Assess this cell for malaria.
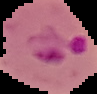
Parasitized.

preparation = thin blood film
image type = cell region segmented out of the field of view; surrounding area masked to black
image size = 97×94 pixels